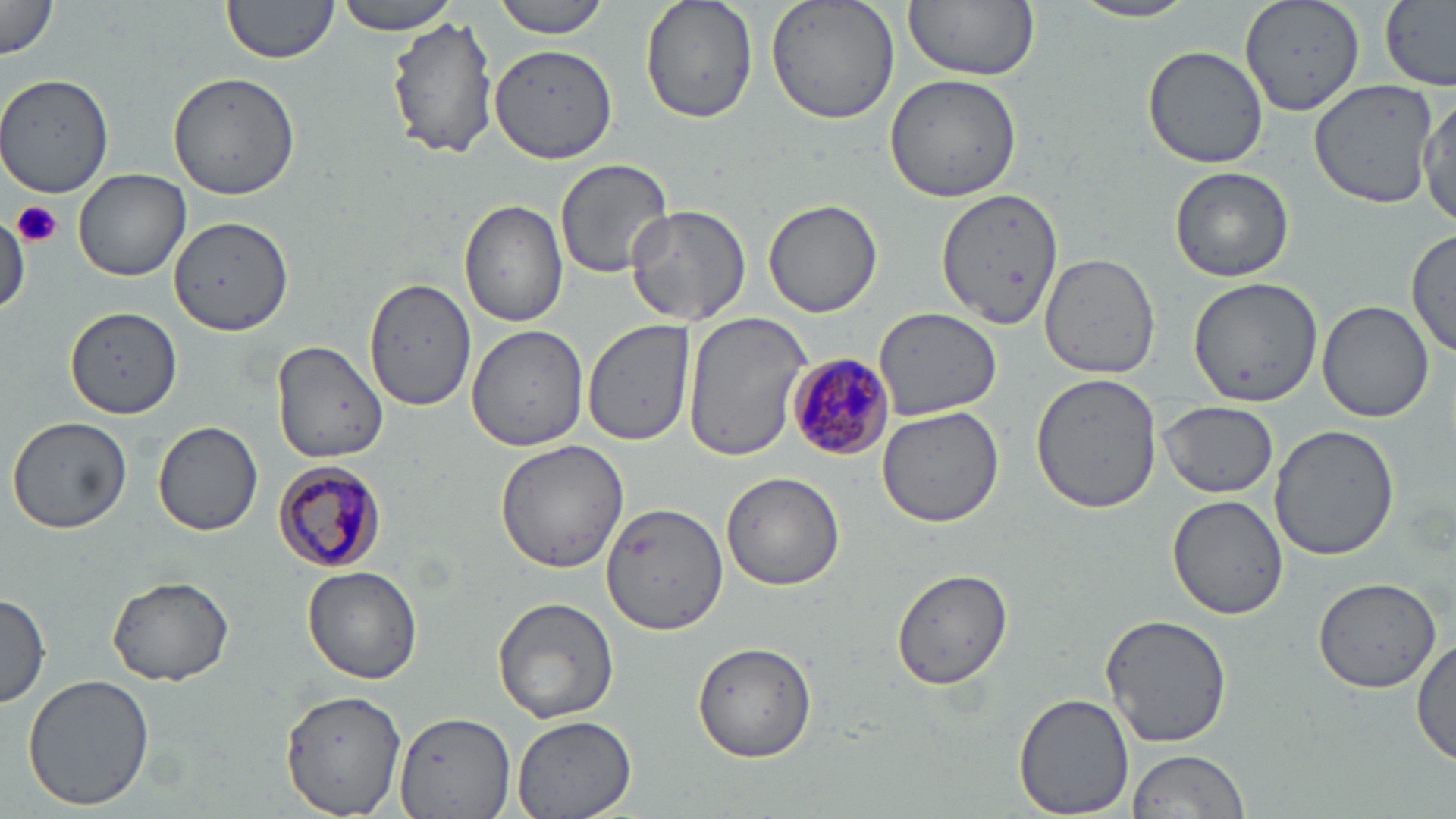

Approximate bounding boxes as (x1, y1, x2, y2) in pixels. Uninfected red blood cell locations: (221, 0, 341, 69), (329, 0, 461, 34), (492, 0, 614, 38), (640, 0, 758, 124), (765, 0, 901, 126), (904, 0, 1041, 82), (1240, 0, 1365, 117), (1378, 0, 1456, 89), (0, 1, 60, 63), (1070, 1, 1201, 24), (385, 13, 499, 163), (490, 45, 619, 165), (1141, 45, 1270, 169), (168, 71, 300, 201), (0, 72, 118, 196), (884, 73, 1024, 205), (1309, 77, 1437, 207), (1419, 94, 1455, 229), (554, 157, 673, 280), (1169, 165, 1294, 282), (74, 168, 192, 282), (936, 189, 1062, 329), (458, 199, 569, 328), (764, 200, 884, 318), (625, 202, 752, 326), (169, 215, 293, 336), (0, 219, 28, 315), (1407, 228, 1455, 360), (1040, 250, 1162, 378), (1188, 278, 1323, 406), (367, 279, 477, 411), (1318, 300, 1435, 422), (67, 307, 182, 418), (875, 307, 1000, 419), (682, 313, 812, 462), (584, 319, 698, 446), (466, 324, 588, 452), (271, 340, 391, 464), (1031, 373, 1163, 515), (1158, 401, 1278, 497), (876, 405, 1004, 528), (7, 416, 132, 535), (152, 418, 264, 537), (1270, 425, 1400, 559), (495, 439, 630, 574), (721, 471, 845, 591), (1168, 494, 1286, 620), (601, 500, 729, 635), (302, 566, 424, 684), (890, 568, 1014, 691), (108, 575, 235, 684), (1313, 577, 1441, 692), (0, 594, 50, 709), (492, 594, 621, 723), (1100, 613, 1232, 750), (1412, 636, 1455, 770), (693, 641, 817, 763), (22, 674, 156, 811), (281, 688, 406, 816), (1014, 692, 1135, 818), (393, 713, 514, 819), (513, 715, 637, 819), (1124, 749, 1251, 818). Plasmodium malariae-infected red blood cell locations: (788, 352, 896, 459), (272, 462, 389, 572). Platelet locations: (13, 201, 63, 248). Slide-level diagnosis: Plasmodium malariae. May-Grünwald-Giemsa-stained preparation. Light microscopy. Thin blood film. Image is 1456×819 pixels. One field of a larger specimen. Captured at 1000x magnification.